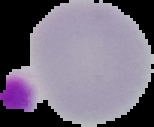

From a thin blood smear. Segmented cell region on a black background. Result: no Plasmodium parasites seen. Image is 154×127 pixels.